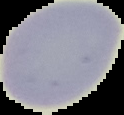
result = no malaria parasites detected
image type = segmented cell region with the area outside set to black
preparation = thin blood smear
image size = 124×115 pixels